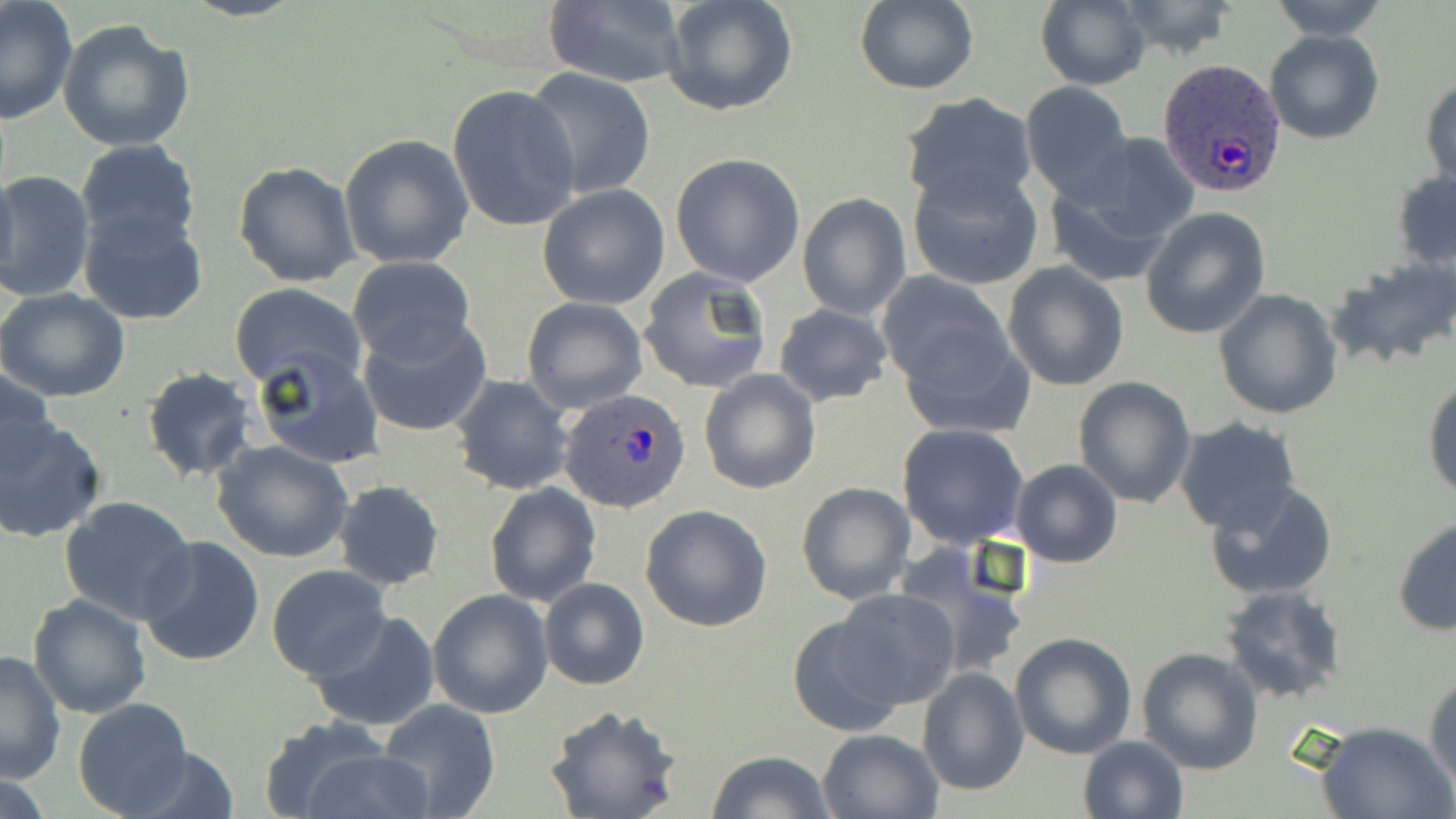

Summary:
  - Coordinate format: approximate bounding boxes as (x1,y1)-(x2,y2) corner pairs in pixels
  - Uninfected red blood cell locations: (661,0)-(799,117), (1035,0)-(1153,90), (1116,0)-(1241,59), (1266,0)-(1390,42), (1,1)-(80,126), (539,1)-(688,88), (855,1)-(979,96), (58,18)-(194,152), (1264,29)-(1386,145), (525,68)-(656,199), (1421,72)-(1455,195), (1019,81)-(1133,202), (446,84)-(581,234), (900,94)-(1038,212), (1078,132)-(1199,244), (339,134)-(474,269), (75,140)-(202,253), (669,152)-(806,286), (1044,159)-(1185,282), (233,160)-(362,288), (907,165)-(1043,291), (0,170)-(95,302), (1391,171)-(1456,272), (537,184)-(670,310), (797,192)-(912,321), (78,207)-(208,326), (1140,207)-(1271,338), (347,256)-(476,368), (1328,257)-(1456,370), (1001,263)-(1129,391), (637,266)-(772,394), (877,270)-(1014,391), (228,284)-(369,391), (0,287)-(131,404), (1214,289)-(1343,419), (521,297)-(649,413), (774,304)-(891,407), (358,315)-(491,437), (894,319)-(1035,440), (253,347)-(382,470), (2,366)-(59,478), (142,366)-(259,482), (698,368)-(821,495), (450,374)-(576,496), (1424,375)-(1456,500), (1073,376)-(1197,507), (0,415)-(105,543), (1173,417)-(1302,537), (897,422)-(1029,549), (211,439)-(354,565), (1011,459)-(1122,567), (333,480)-(446,591), (483,480)-(602,609), (1204,481)-(1339,601), (797,482)-(916,605), (59,494)-(195,623), (640,503)-(772,633), (1392,517)-(1456,635), (137,534)-(267,666), (898,549)-(1029,681), (266,564)-(392,681), (538,575)-(650,690), (1220,584)-(1347,702), (426,589)-(554,719), (833,589)-(961,710), (28,593)-(154,718), (310,609)-(441,732), (786,612)-(909,739), (1009,631)-(1138,758), (1136,647)-(1262,774), (0,650)-(66,784), (917,666)-(1029,796), (1425,674)-(1456,796), (73,699)-(194,818), (376,699)-(501,819), (544,704)-(682,819), (256,720)-(391,819), (1314,720)-(1454,819), (817,727)-(945,819), (1078,736)-(1189,819), (119,745)-(242,819), (297,748)-(436,819), (707,749)-(838,819), (0,769)-(59,819)
  - Plasmodium ovale-infected red blood cell locations: (1158,59)-(1287,195), (561,390)-(690,514)
  - Slide-level diagnosis: Plasmodium ovale
  - Magnification: 1000x
  - Image size: 1456×819 pixels
  - Field of view: one of a larger specimen
  - Stain: May-Grünwald-Giemsa
  - Preparation: thin blood film
  - Modality: optical microscopy